Mark where platelets are.
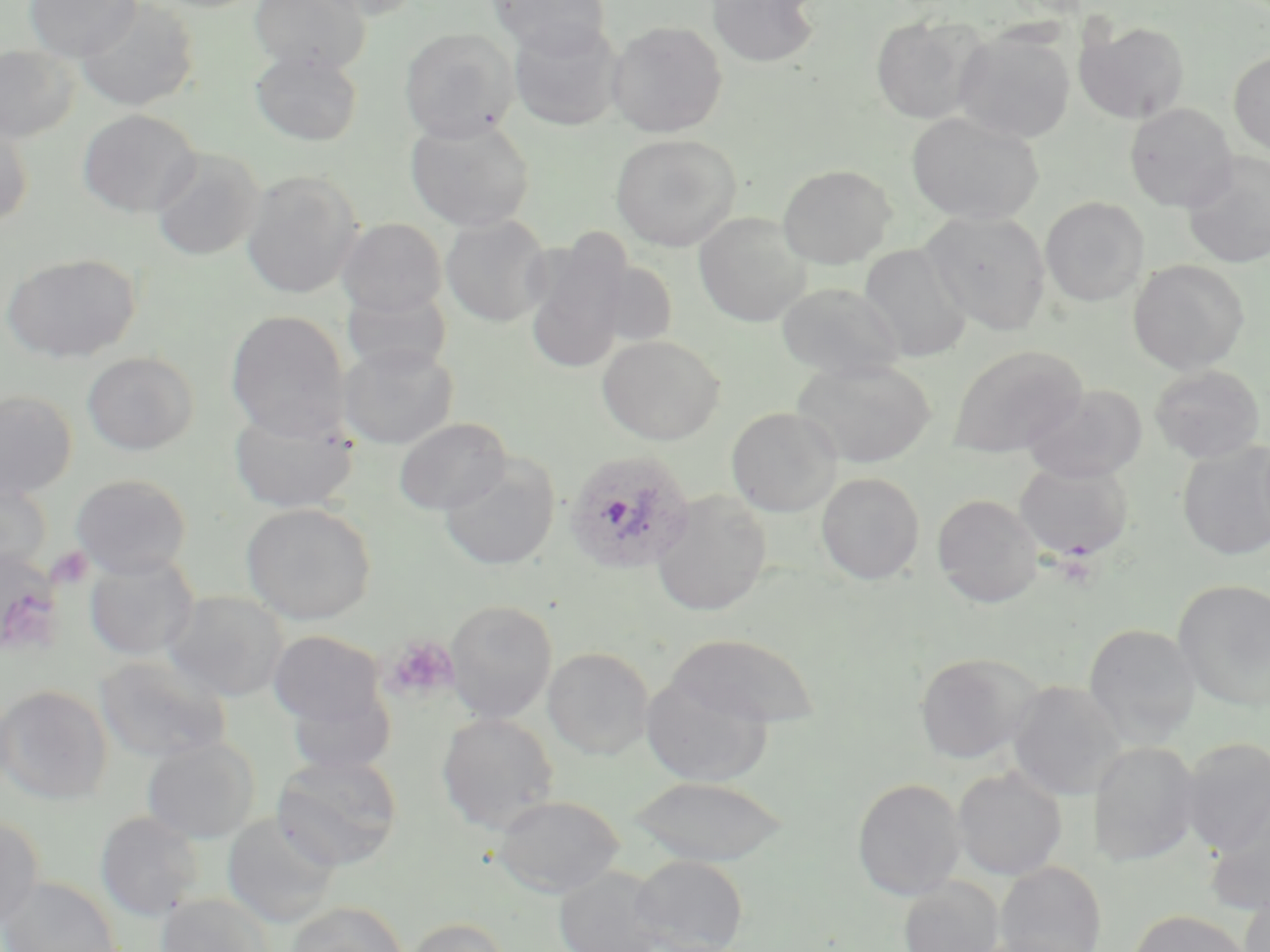
Approximate bounding boxes as (x1,y1)-(x2,y2) corner pairs in pixels.
Platelets: (49,547)-(93,589), (0,552)-(66,658), (385,636)-(458,702).

{
  "slide_level_diagnosis": "Plasmodium ovale",
  "magnification": "1000x",
  "plasmodium_ovale_infected_red_blood_cell_locations": "approximate bounding boxes as (x1,y1)-(x2,y2) corner pairs in pixels: (562,448)-(697,576)",
  "uninfected_red_blood_cell_locations": "approximate bounding boxes as (x1,y1)-(x2,y2) corner pairs in pixels: (24,0)-(141,61), (74,0)-(200,112), (249,0)-(370,74), (311,0)-(425,21), (487,0)-(611,55), (706,0)-(820,68), (871,16)-(985,123), (508,18)-(624,131), (607,20)-(727,137), (1076,21)-(1190,124), (953,27)-(1076,144), (399,28)-(518,142), (0,44)-(78,143), (250,49)-(363,147), (1229,51)-(1270,155), (1125,103)-(1238,212), (77,109)-(201,218), (906,111)-(1044,226), (0,116)-(33,229), (406,118)-(536,231), (610,133)-(742,251), (150,148)-(264,262), (1182,152)-(1270,269), (777,164)-(896,268), (240,169)-(363,299), (1041,197)-(1148,306), (922,210)-(1052,336), (694,212)-(811,327), (441,214)-(552,327), (337,218)-(447,319), (523,237)-(632,375), (859,244)-(972,362), (2,252)-(141,363), (1128,259)-(1249,374), (591,260)-(680,348), (777,281)-(904,380), (342,287)-(452,379), (226,310)-(350,440), (598,335)-(725,446), (338,344)-(459,448), (947,344)-(1088,458), (82,351)-(199,455), (792,358)-(937,468), (1150,365)-(1267,463), (1022,384)-(1148,483), (0,389)-(78,501), (229,406)-(358,514), (726,407)-(843,516), (394,417)-(511,515), (1177,441)-(1270,560), (439,456)-(560,571), (1014,459)-(1134,561), (816,472)-(924,584), (70,473)-(192,578), (0,476)-(53,578), (650,491)-(772,616), (932,493)-(1043,607), (241,503)-(376,625), (0,549)-(63,655), (84,554)-(199,661), (1173,579)-(1270,712), (162,590)-(289,702), (445,599)-(558,723), (1083,623)-(1201,747), (268,629)-(387,729), (666,633)-(821,730), (543,647)-(654,759), (914,652)-(1040,764), (95,655)-(232,763), (1037,656)-(1162,782), (641,674)-(774,786), (1007,681)-(1126,800), (0,684)-(112,805), (286,684)-(397,778), (437,711)-(559,833), (142,736)-(260,843), (1179,737)-(1269,855), (1090,741)-(1201,867), (271,753)-(403,871), (953,767)-(1067,881), (627,776)-(791,866), (852,778)-(965,900), (491,794)-(624,898), (1204,802)-(1270,916), (95,812)-(203,922), (0,814)-(43,931), (221,814)-(340,928), (630,855)-(748,952), (995,861)-(1106,952), (554,866)-(668,952), (0,876)-(122,952), (898,878)-(1004,952), (1239,890)-(1269,952), (156,892)-(273,951), (285,900)-(409,952), (1129,909)-(1252,952), (405,916)-(510,952), (971,934)-(1095,952)",
  "field_of_view": "single",
  "modality": "light microscopy",
  "preparation": "thin blood film",
  "image_size": "1270×952 pixels",
  "stain": "May-Grünwald-Giemsa"
}